Report the malaria status of this cell.
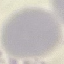

Uninfected.

stain = Giemsa
image type = automatically extracted cell patch, resized to 64 × 64 pixels
preparation = thin blood film
capture = smartphone through the microscope eyepiece